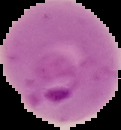
Summary:
  - Preparation: thin blood film
  - Image type: segmented cell region with the area outside set to black
  - Image size: 121×130 pixels
  - Malaria status: parasitized